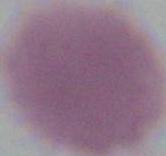

{
  "modality": "photomicrograph",
  "identification": "red blood cell",
  "magnification": "1000x"
}